Give the extent of all Plasmodium ovale-infected red blood cells.
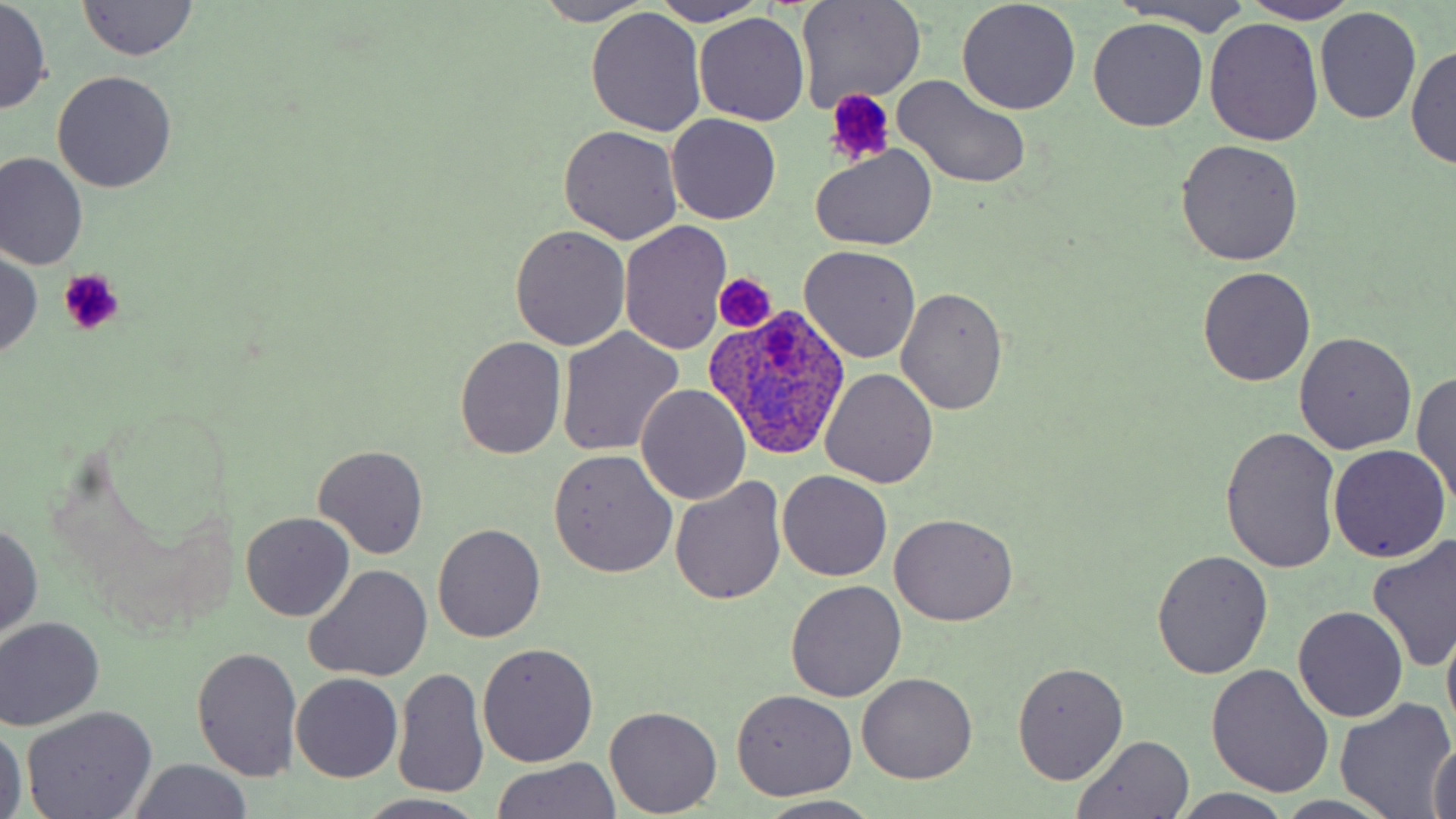
Approximate bounding boxes as named x1/y1/x2/y2 corners in pixels.
Plasmodium ovale-infected red blood cells: (x1=706, y1=304, x2=851, y2=462).

Summary:
  - Platelet locations: (x1=825, y1=89, x2=895, y2=164), (x1=59, y1=268, x2=126, y2=336), (x1=714, y1=274, x2=775, y2=330)
  - Uninfected red blood cell locations: (x1=795, y1=0, x2=927, y2=111), (x1=1108, y1=0, x2=1258, y2=36), (x1=1, y1=1, x2=51, y2=113), (x1=77, y1=1, x2=199, y2=60), (x1=650, y1=1, x2=768, y2=26), (x1=1246, y1=1, x2=1360, y2=23), (x1=532, y1=2, x2=657, y2=25), (x1=956, y1=2, x2=1082, y2=115), (x1=1314, y1=7, x2=1422, y2=124), (x1=586, y1=9, x2=706, y2=136), (x1=694, y1=13, x2=808, y2=126), (x1=1088, y1=18, x2=1210, y2=132), (x1=1204, y1=19, x2=1323, y2=146), (x1=1408, y1=44, x2=1455, y2=170), (x1=52, y1=70, x2=176, y2=192), (x1=894, y1=75, x2=1032, y2=190), (x1=667, y1=113, x2=781, y2=224), (x1=558, y1=124, x2=683, y2=245), (x1=1175, y1=139, x2=1305, y2=265), (x1=812, y1=144, x2=935, y2=249), (x1=0, y1=154, x2=88, y2=272), (x1=621, y1=221, x2=732, y2=354), (x1=509, y1=226, x2=631, y2=350), (x1=800, y1=245, x2=921, y2=364), (x1=0, y1=251, x2=44, y2=359), (x1=1197, y1=267, x2=1317, y2=387), (x1=895, y1=286, x2=1007, y2=413), (x1=557, y1=327, x2=684, y2=455), (x1=1293, y1=334, x2=1416, y2=455), (x1=454, y1=336, x2=567, y2=458), (x1=822, y1=368, x2=940, y2=488), (x1=1411, y1=369, x2=1456, y2=508), (x1=637, y1=383, x2=752, y2=505), (x1=1221, y1=426, x2=1341, y2=574), (x1=313, y1=445, x2=428, y2=560), (x1=1329, y1=446, x2=1450, y2=563), (x1=548, y1=449, x2=677, y2=578), (x1=777, y1=470, x2=892, y2=581), (x1=672, y1=478, x2=785, y2=603), (x1=241, y1=512, x2=354, y2=621), (x1=889, y1=512, x2=1020, y2=625), (x1=0, y1=520, x2=44, y2=640), (x1=433, y1=523, x2=544, y2=643), (x1=1367, y1=536, x2=1456, y2=673), (x1=1151, y1=551, x2=1273, y2=680), (x1=305, y1=563, x2=433, y2=682), (x1=786, y1=580, x2=907, y2=701), (x1=1293, y1=606, x2=1408, y2=723), (x1=0, y1=617, x2=104, y2=729), (x1=1442, y1=617, x2=1456, y2=744), (x1=4, y1=626, x2=132, y2=814), (x1=478, y1=643, x2=598, y2=768), (x1=193, y1=646, x2=303, y2=779), (x1=1205, y1=662, x2=1334, y2=798), (x1=1012, y1=663, x2=1129, y2=784), (x1=394, y1=667, x2=489, y2=802), (x1=857, y1=672, x2=978, y2=785), (x1=293, y1=673, x2=402, y2=782), (x1=731, y1=689, x2=857, y2=800), (x1=1337, y1=698, x2=1454, y2=817), (x1=606, y1=707, x2=721, y2=816), (x1=22, y1=708, x2=156, y2=819), (x1=0, y1=722, x2=26, y2=819), (x1=1070, y1=735, x2=1196, y2=818), (x1=1429, y1=738, x2=1456, y2=819), (x1=487, y1=759, x2=623, y2=817), (x1=126, y1=760, x2=256, y2=817), (x1=1171, y1=790, x2=1298, y2=819), (x1=360, y1=793, x2=487, y2=818), (x1=754, y1=796, x2=884, y2=819)
  - Slide-level diagnosis: Plasmodium ovale
  - Image size: 1456×819 pixels
  - Preparation: thin blood smear
  - Magnification: 1000x
  - Stain: May-Grünwald-Giemsa
  - Modality: optical microscopy
  - Field of view: one of a larger specimen